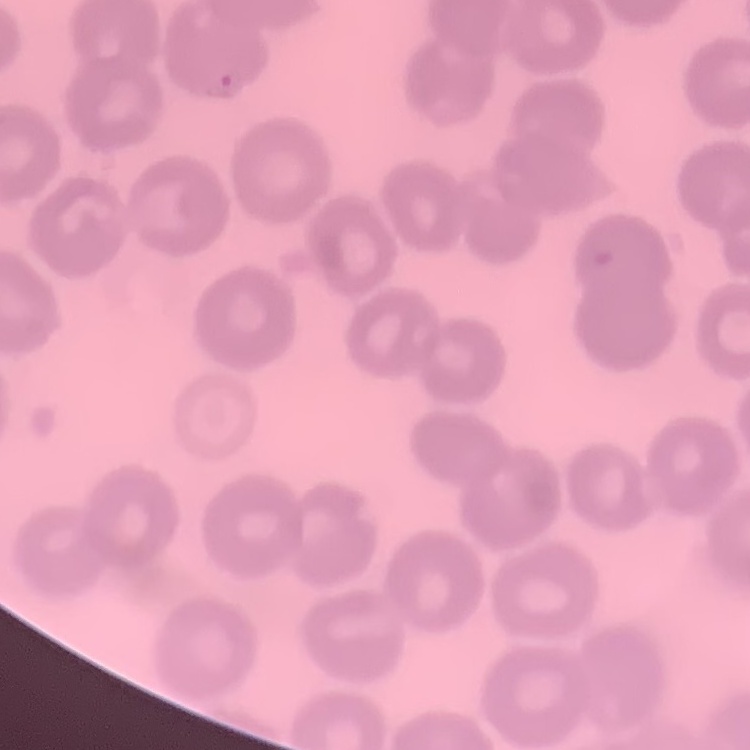
erythrocyte morphology = no rouleaux formation
preparation = thin blood smear
image type = square crop of a larger photomicrograph
stain = Field's or Giemsa